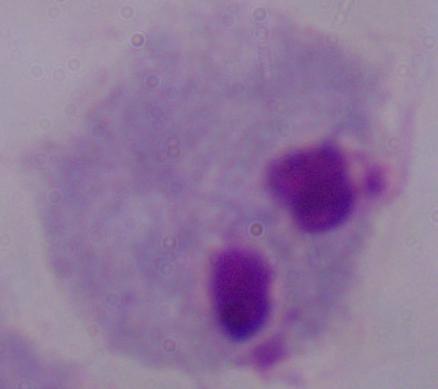

Summary:
  - Modality: micrograph
  - Magnification: 1000x
  - Identification: trichomonad